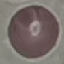
Summary:
  - Result: no malaria parasites detected
  - Capture: smartphone camera at the microscope eyepiece
  - Image type: automatically extracted cell patch, resized to 64 × 64 pixels
  - Stain: Giemsa
  - Preparation: thin blood smear